Locate every uninfected red blood cell.
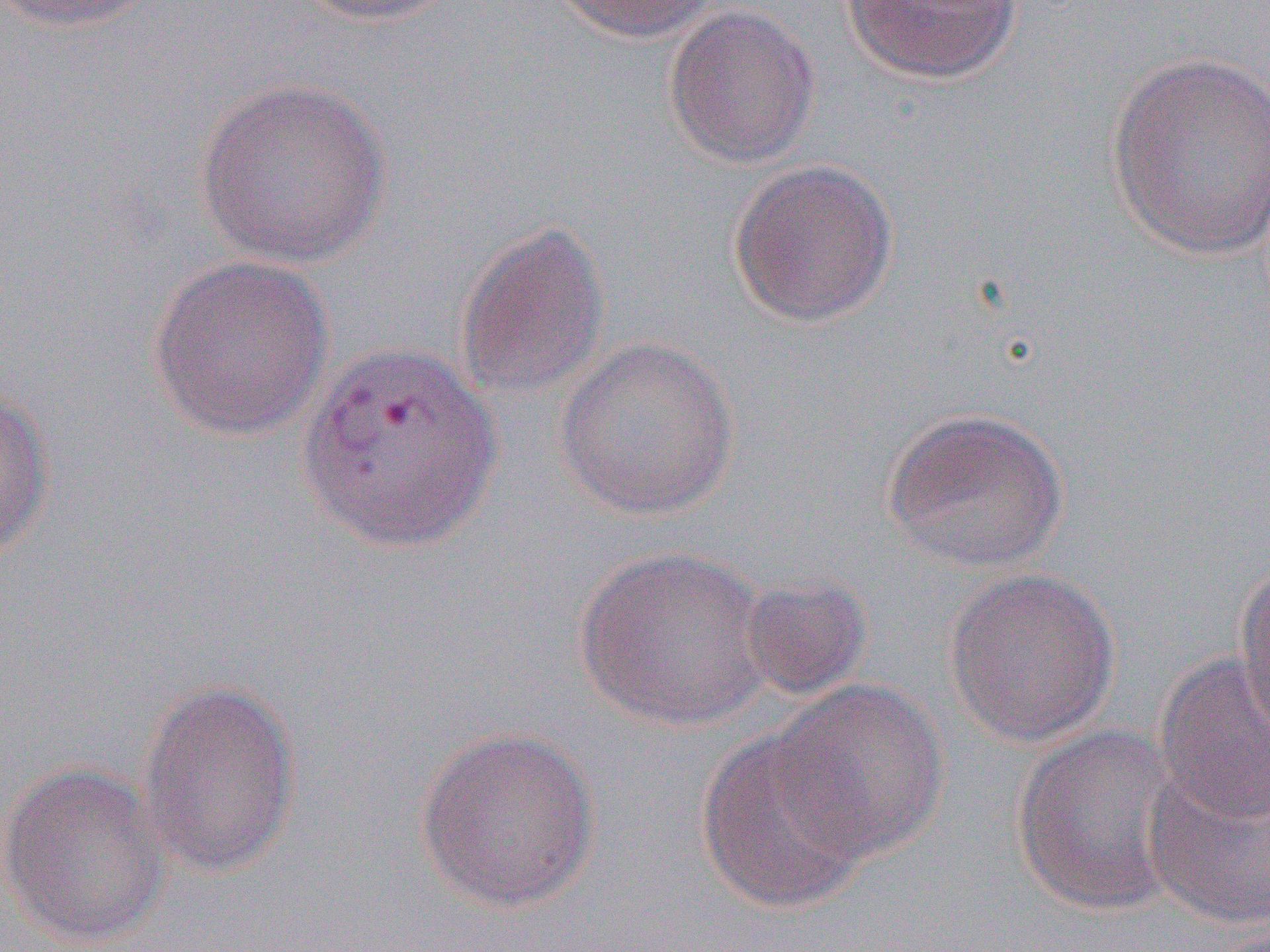
Approximate bounding boxes as [x1, y1, x2, y2] in pixels.
Uninfected red blood cells: [4, 0, 162, 32], [290, 0, 460, 27], [547, 0, 720, 42], [839, 0, 1023, 85], [663, 4, 822, 170], [1103, 50, 1270, 261], [193, 77, 392, 269], [727, 159, 899, 328], [455, 219, 613, 403], [146, 254, 336, 442], [553, 335, 740, 523], [297, 339, 501, 556], [0, 385, 57, 562], [882, 406, 1071, 575], [574, 544, 775, 733], [1233, 557, 1270, 747], [942, 567, 1121, 749], [737, 573, 874, 702], [1152, 653, 1269, 825], [136, 678, 303, 880], [773, 679, 949, 863], [1010, 723, 1187, 917], [413, 725, 602, 913], [695, 728, 875, 914], [1141, 760, 1269, 931], [0, 761, 171, 949].

Slide-level diagnosis: Plasmodium vivax. Image is 1270×952 pixels. Single field of view. Thin blood smear. Captured at 1000x magnification. Light microscopy.